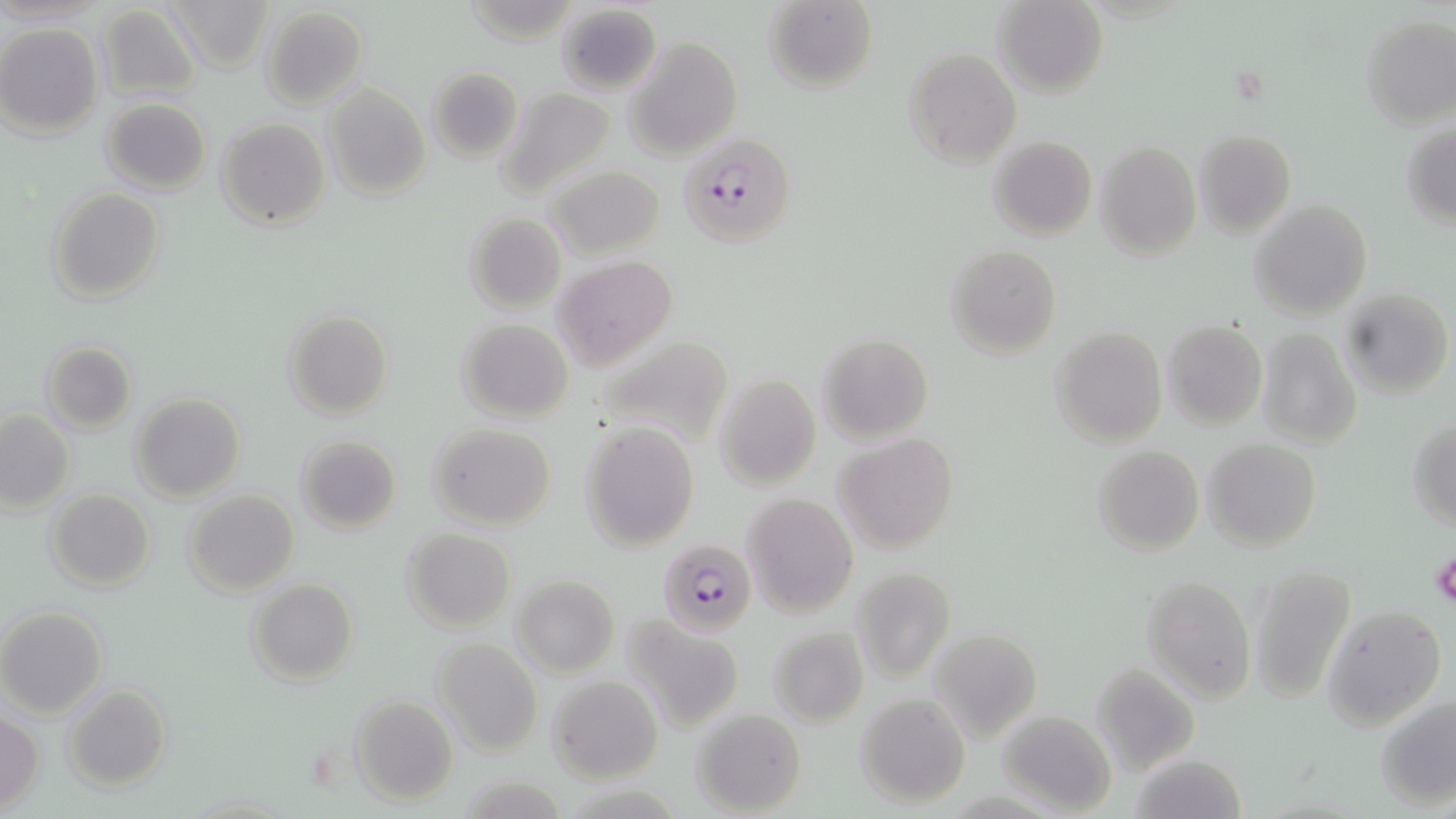

Summary:
  - Coordinate format: approximate bounding boxes as [x1, y1, x2, y2] in pixels
  - Plasmodium falciparum-infected red blood cell locations: [678, 132, 797, 249], [660, 538, 757, 636]
  - Uninfected red blood cell locations: [164, 0, 275, 74], [762, 0, 878, 93], [993, 0, 1109, 98], [554, 2, 662, 94], [96, 4, 204, 102], [261, 6, 368, 111], [1359, 13, 1456, 128], [0, 23, 104, 139], [625, 36, 742, 160], [903, 47, 1022, 170], [426, 66, 523, 161], [324, 82, 431, 202], [495, 85, 619, 201], [101, 98, 212, 194], [217, 117, 328, 231], [1401, 118, 1456, 235], [1195, 128, 1296, 237], [988, 135, 1096, 241], [1095, 140, 1202, 261], [545, 164, 666, 260], [47, 188, 164, 305], [1248, 199, 1373, 320], [464, 211, 566, 316], [944, 244, 1062, 358], [551, 256, 677, 369], [1339, 288, 1453, 401], [283, 307, 394, 420], [457, 318, 574, 423], [1161, 319, 1268, 431], [1050, 325, 1167, 448], [1254, 327, 1363, 451], [591, 333, 736, 448], [817, 333, 935, 443], [40, 341, 137, 434], [713, 373, 821, 491], [133, 393, 245, 502], [0, 408, 75, 514], [1407, 415, 1456, 529], [579, 419, 700, 552], [429, 424, 555, 531], [295, 434, 402, 533], [835, 434, 959, 554], [1202, 438, 1321, 551], [1092, 445, 1204, 556], [47, 489, 156, 592], [183, 489, 300, 598], [741, 492, 859, 620], [401, 527, 516, 633], [1248, 563, 1356, 703], [848, 565, 958, 686], [1144, 572, 1256, 700], [511, 576, 620, 677], [248, 578, 359, 686], [1324, 605, 1447, 727], [0, 607, 107, 718], [622, 616, 743, 731], [769, 625, 868, 728], [933, 631, 1043, 744], [432, 638, 542, 756], [1090, 661, 1200, 775], [549, 675, 664, 783], [63, 684, 172, 792], [854, 693, 972, 809], [1375, 693, 1455, 811], [349, 695, 459, 807], [692, 707, 807, 816], [997, 712, 1117, 814], [1, 713, 44, 812]
  - Platelet locations: [1431, 554, 1456, 608]
  - Slide-level diagnosis: Plasmodium falciparum
  - Stain: May-Grünwald-Giemsa
  - Image size: 1456×819 pixels
  - Modality: light microscopy
  - Field of view: one of a larger specimen
  - Magnification: 1000x
  - Preparation: thin blood smear